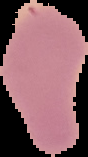

{
  "preparation": "thin blood film",
  "image_type": "cell region segmented out of the field of view; surrounding area masked to black",
  "image_size": "88×157 pixels",
  "result": "negative for Plasmodium parasites"
}